Report the malaria status of this cell.
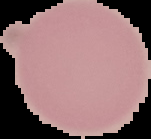

It is uninfected.

From a thin blood smear. Segmented cell region on a black background. Image is 151×139 pixels.